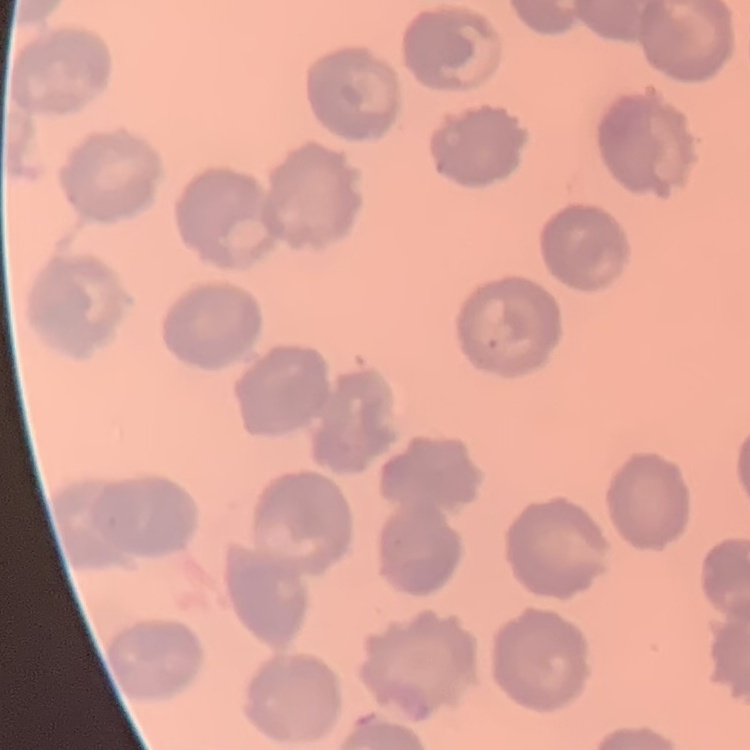 The red blood cells exhibit no rouleaux formation. Stained with either Field's or Giemsa. One tile cut from a larger photomicrograph. Thin blood film.